Name the blood parasite species.
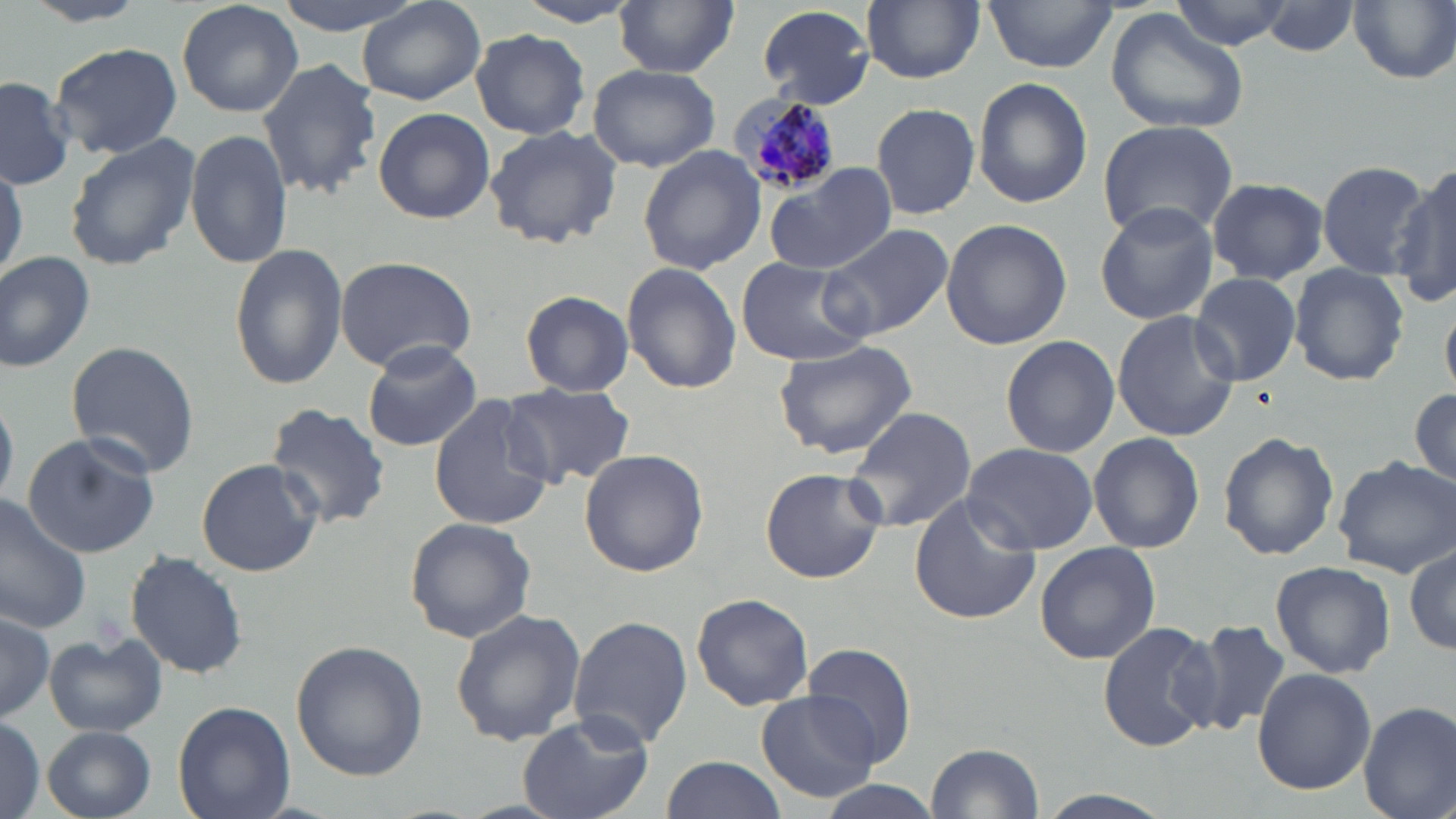

Plasmodium malariae.

uninfected_red_blood_cell_locations: 'approximate bounding boxes as named x1/y1/x2/y2 corners in pixels: (x1=19, y1=0, x2=155, y2=26), (x1=175, y1=0, x2=305, y2=119), (x1=274, y1=0, x2=425, y2=35), (x1=861, y1=0, x2=985, y2=83), (x1=1168, y1=0, x2=1294, y2=51), (x1=359, y1=1, x2=485, y2=107), (x1=983, y1=1, x2=1118, y2=73), (x1=511, y1=2, x2=642, y2=27), (x1=614, y1=2, x2=738, y2=77), (x1=1349, y1=2, x2=1456, y2=86), (x1=1263, y1=3, x2=1362, y2=57), (x1=755, y1=4, x2=876, y2=108), (x1=1104, y1=7, x2=1249, y2=135), (x1=471, y1=29, x2=591, y2=140), (x1=48, y1=42, x2=184, y2=161), (x1=257, y1=58, x2=382, y2=200), (x1=587, y1=64, x2=723, y2=172), (x1=0, y1=74, x2=76, y2=191), (x1=971, y1=77, x2=1093, y2=210), (x1=871, y1=102, x2=981, y2=219), (x1=373, y1=107, x2=495, y2=223), (x1=1097, y1=120, x2=1239, y2=242), (x1=483, y1=125, x2=623, y2=249), (x1=185, y1=126, x2=292, y2=271), (x1=64, y1=134, x2=199, y2=271), (x1=636, y1=144, x2=767, y2=278), (x1=0, y1=157, x2=24, y2=284), (x1=1316, y1=159, x2=1432, y2=277), (x1=761, y1=161, x2=897, y2=277), (x1=1392, y1=164, x2=1456, y2=287), (x1=1207, y1=176, x2=1327, y2=283), (x1=1094, y1=201, x2=1218, y2=324), (x1=940, y1=218, x2=1072, y2=351), (x1=821, y1=223, x2=952, y2=339), (x1=228, y1=243, x2=347, y2=389), (x1=0, y1=250, x2=96, y2=373), (x1=334, y1=256, x2=477, y2=371), (x1=735, y1=257, x2=875, y2=367), (x1=623, y1=261, x2=741, y2=394), (x1=1289, y1=266, x2=1410, y2=387), (x1=1190, y1=271, x2=1302, y2=385), (x1=521, y1=290, x2=633, y2=396), (x1=1110, y1=311, x2=1240, y2=441), (x1=1000, y1=335, x2=1119, y2=459), (x1=774, y1=337, x2=918, y2=460), (x1=361, y1=339, x2=482, y2=453), (x1=65, y1=341, x2=200, y2=476), (x1=502, y1=383, x2=633, y2=488), (x1=1409, y1=383, x2=1455, y2=492), (x1=428, y1=392, x2=558, y2=532), (x1=265, y1=403, x2=392, y2=531), (x1=845, y1=406, x2=978, y2=534), (x1=1217, y1=430, x2=1339, y2=561), (x1=22, y1=432, x2=160, y2=560), (x1=1087, y1=432, x2=1206, y2=553), (x1=961, y1=442, x2=1098, y2=555), (x1=580, y1=449, x2=709, y2=576), (x1=1333, y1=457, x2=1456, y2=577), (x1=195, y1=459, x2=323, y2=578), (x1=759, y1=467, x2=886, y2=585), (x1=908, y1=494, x2=1041, y2=627), (x1=0, y1=495, x2=92, y2=634), (x1=403, y1=516, x2=537, y2=644), (x1=1034, y1=540, x2=1161, y2=665), (x1=1405, y1=542, x2=1456, y2=657), (x1=125, y1=550, x2=248, y2=679), (x1=1270, y1=560, x2=1395, y2=679), (x1=691, y1=592, x2=815, y2=712), (x1=450, y1=607, x2=586, y2=746), (x1=0, y1=611, x2=55, y2=721), (x1=567, y1=615, x2=692, y2=750), (x1=1179, y1=618, x2=1294, y2=737), (x1=1098, y1=620, x2=1219, y2=753), (x1=44, y1=633, x2=167, y2=736), (x1=290, y1=640, x2=427, y2=780), (x1=805, y1=643, x2=916, y2=766), (x1=1252, y1=667, x2=1376, y2=795), (x1=757, y1=689, x2=880, y2=803), (x1=170, y1=699, x2=296, y2=819), (x1=1358, y1=701, x2=1456, y2=819), (x1=515, y1=712, x2=656, y2=819), (x1=0, y1=715, x2=46, y2=819), (x1=41, y1=725, x2=157, y2=819), (x1=924, y1=742, x2=1044, y2=818), (x1=660, y1=755, x2=787, y2=819)'
magnification: 1000x
modality: optical microscopy
stain: May-Grünwald-Giemsa
image_size: 1456×819 pixels
preparation: thin blood film
field_of_view: one of a larger specimen
plasmodium_malariae_infected_red_blood_cell_locations: 'approximate bounding boxes as named x1/y1/x2/y2 corners in pixels: (x1=728, y1=96, x2=838, y2=196)'